Report the malaria status of this cell.
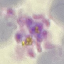

Parasitized.

Thin smear of blood. Cell patch, automatically extracted from a larger field of view and resized to 64 × 64 pixels. Giemsa stain. Acquired by smartphone through the microscope eyepiece.